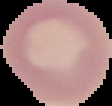
Summary:
  - Image type: segmented cell region with the area outside set to black
  - Result: no malaria parasites detected
  - Image size: 112×106 pixels
  - Preparation: thin blood smear